Assess this cell for malaria.
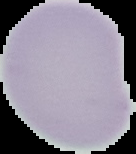
It is uninfected.

image type = cell region segmented out of the field of view; surrounding area masked to black
image size = 136×154 pixels
preparation = thin blood film